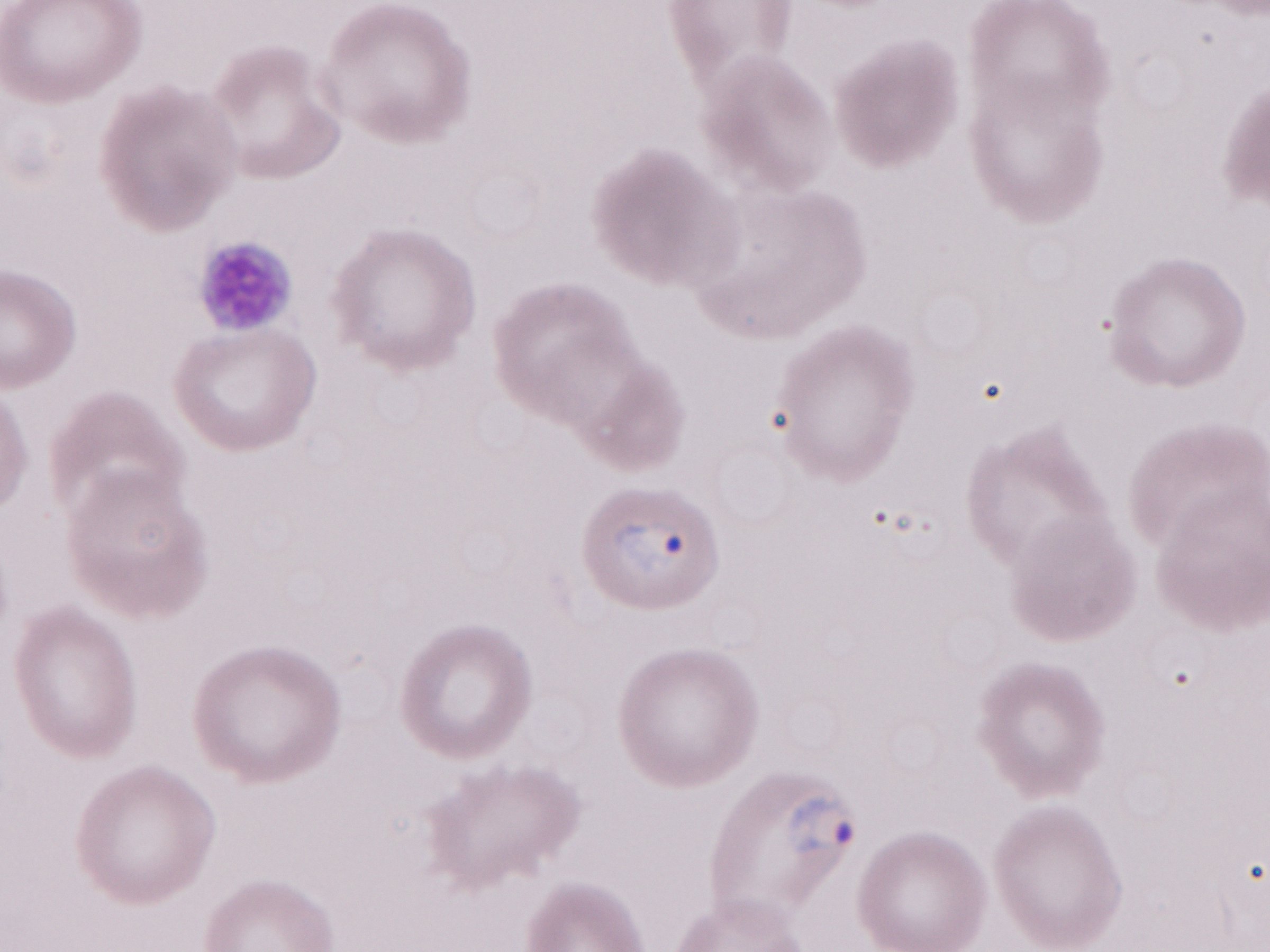 Malaria diagnosis (patient-level): positive. May-Grünwald-Giemsa stain. Image is 1270×952 pixels. Olympus BX43 microscope, Olympus DP73 camera. Magnification: 1,000x. Thin peripheral-blood smear. Single field of view.